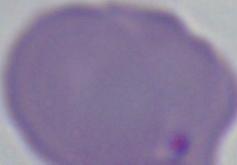

{
  "identification": "Babesia",
  "modality": "micrograph",
  "magnification": "1000x"
}